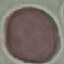
Malaria status: uninfected. Cell patch, automatically extracted from a larger field of view and resized to 64 × 64 pixels. Giemsa-stained preparation. Thin smear of blood. Acquired by smartphone through the microscope eyepiece.